Identify the parasite.
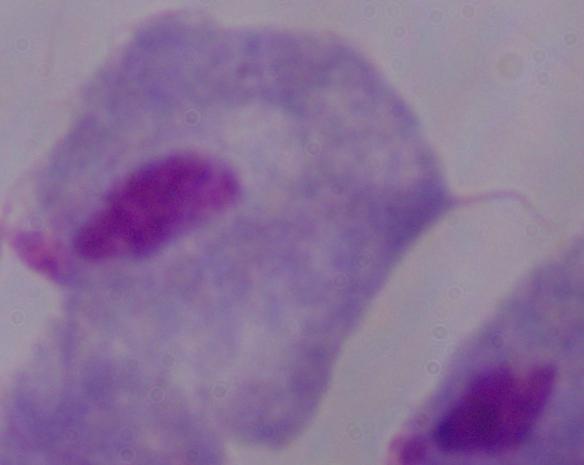
A trichomonad.

Summary:
  - Magnification: 1000x
  - Modality: micrograph